Assess this cell for malaria.
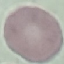

It is uninfected.

Thin smear of blood. Photographed with a smartphone camera at the microscope eyepiece. Cell patch, automatically extracted from a larger field of view and resized to 64 × 64 pixels. Giemsa stain.